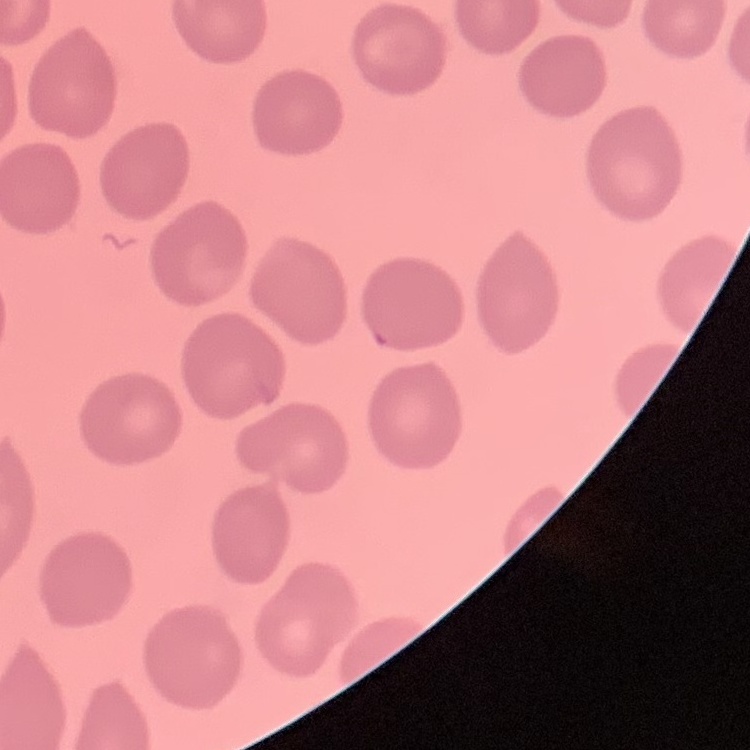

red blood cell morphology = no rouleaux formation
image type = square crop of a larger photomicrograph
stain = Field's or Giemsa
preparation = thin blood film